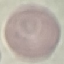
{
  "malaria_status": "uninfected",
  "image_type": "automatically extracted cell patch, resized to 64 × 64 pixels",
  "preparation": "thin blood smear",
  "stain": "Giemsa",
  "capture": "smartphone camera at the microscope eyepiece"
}